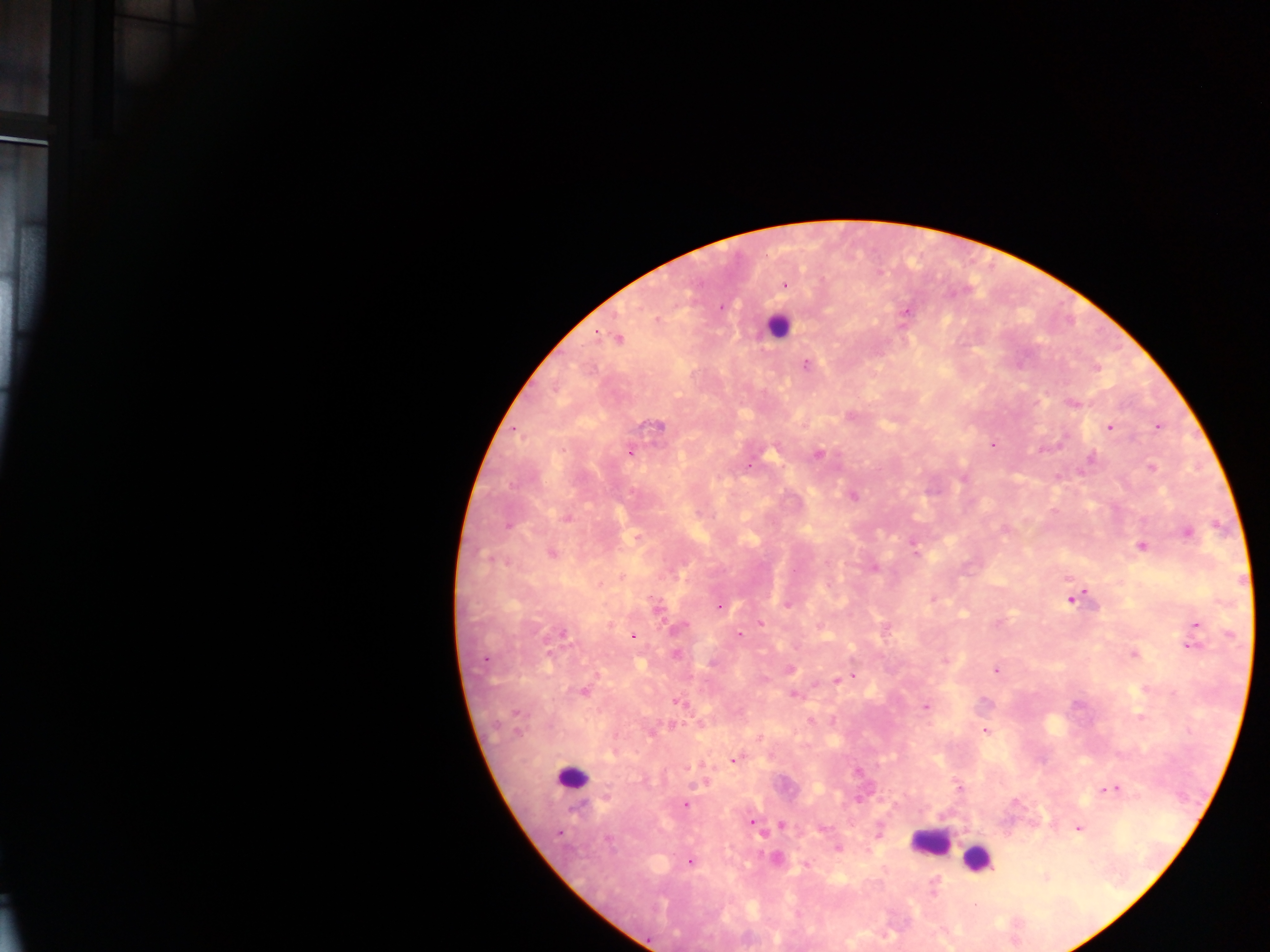

Approximate centers as x y in pixels.
Summary:
  - Malaria parasite locations: 784 285; 719 307; 904 311; 656 321; 618 337; 805 364; 1096 368; 1072 404; 851 416; 1157 425; 656 426; 1108 427; 992 444; 630 451; 818 454; 1090 459; 1151 468; 852 495; 566 517; 508 525; 1187 532; 914 544; 1141 546; 550 553; 874 567; 1072 596; 787 604; 719 606; 657 607; 759 623; 1195 624; 678 627; 561 633; 739 634; 633 636; 1189 646; 676 654; 1133 654; 485 659; 945 661; 789 669; 995 669; 853 676; 842 678; 836 680; 583 691; 794 694; 677 701; 925 706; 984 730; 733 760; 958 788; 1109 788; 684 804; 751 822; 781 825; 1078 827; 837 848; 776 860; 689 861; 806 865; 1045 876
  - Leukocyte locations: 777 326; 572 778; 930 842; 977 859
  - Image size: 1270×952 pixels
  - Capture: mobile-phone photograph through a microscope
  - Country: Ghana
  - Preparation: thick blood smear
  - Field of view: single